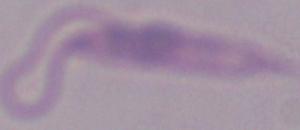
identification: Leishmania
magnification: 1000x
modality: micrograph